Identify the parasite.
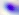

This is Toxoplasma gondii.

Captured at 400x magnification. Photomicrograph.